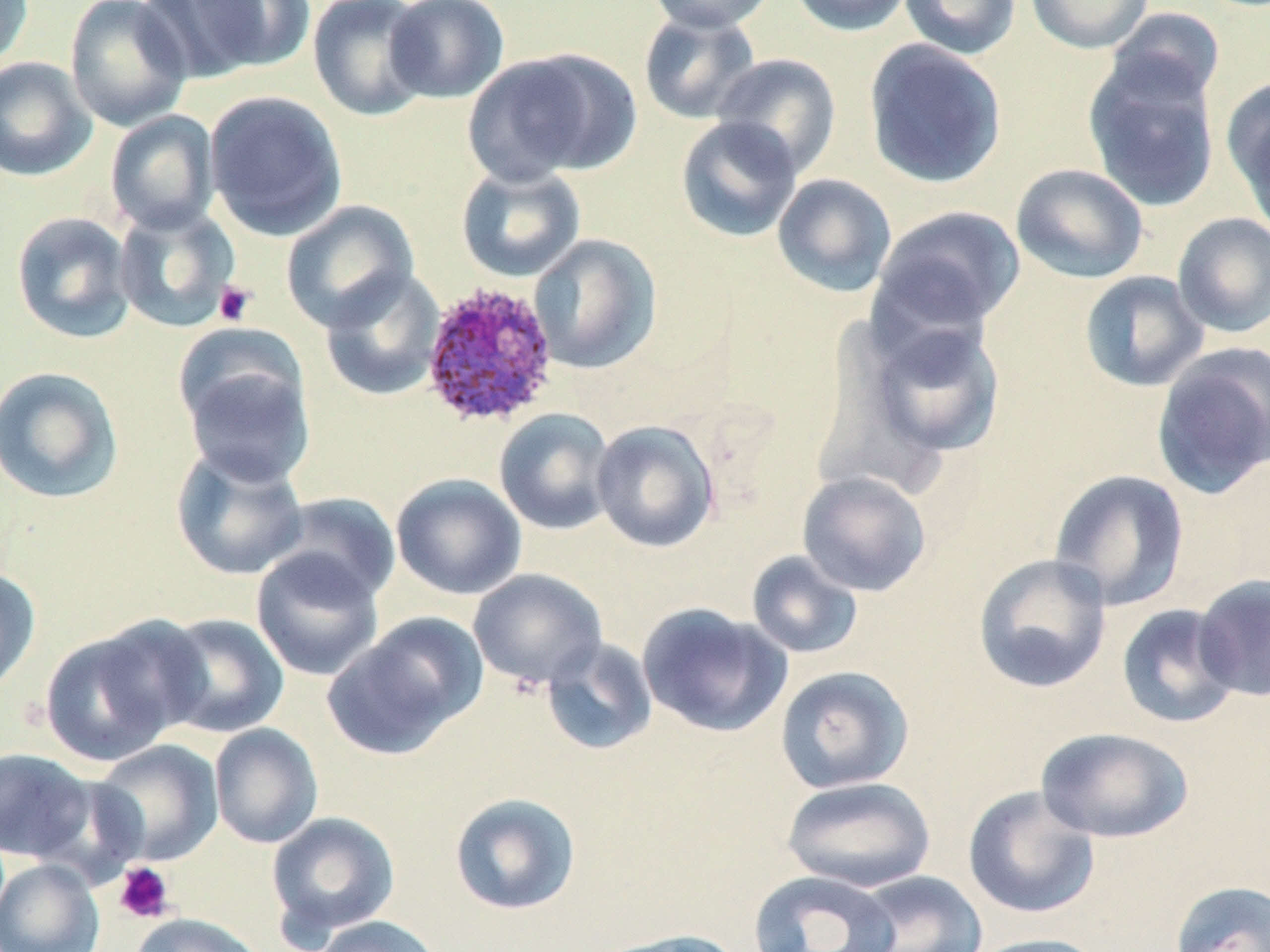
slide-level diagnosis = Plasmodium ovale
modality = optical microscopy
preparation = thin blood smear
field of view = one of a larger specimen
Plasmodium ovale-infected red blood cell locations = approximate bounding boxes as (x1,y1)-(x2,y2) corner pairs in pixels: (420,280)-(560,430)
stain = May-Grünwald-Giemsa
image size = 1270×952 pixels
uninfected red blood cell locations = approximate bounding boxes as (x1,y1)-(x2,y2) corner pairs in pixels: (0,0)-(33,70), (64,0)-(193,131), (152,0)-(314,79), (307,0)-(434,121), (384,0)-(510,104), (645,0)-(777,33), (787,0)-(917,36), (898,0)-(1022,60), (1025,0)-(1153,54), (1107,7)-(1226,107), (638,9)-(761,125), (863,39)-(1007,189), (464,47)-(638,184), (711,52)-(842,176), (0,56)-(97,182), (1083,59)-(1221,213), (1222,77)-(1270,228), (204,90)-(348,240), (104,110)-(220,235), (675,115)-(803,242), (454,162)-(586,282), (1010,163)-(1149,284), (772,173)-(897,297), (280,200)-(419,332), (113,203)-(242,333), (871,205)-(1026,334), (10,210)-(136,344), (1172,212)-(1270,338), (528,233)-(662,373), (319,267)-(446,402), (1079,270)-(1209,392), (854,316)-(1008,462), (1151,342)-(1270,498), (178,343)-(317,488), (0,365)-(125,504), (494,407)-(617,535), (590,420)-(720,553), (170,445)-(309,581), (1048,469)-(1190,611), (797,471)-(932,597), (391,473)-(527,600), (268,491)-(401,606), (250,547)-(385,682), (746,550)-(864,659), (973,553)-(1112,694), (0,566)-(41,695), (468,568)-(608,689), (1193,573)-(1270,702), (637,602)-(790,738), (1116,603)-(1243,729), (155,612)-(289,739), (325,613)-(487,759), (38,619)-(198,768), (540,637)-(659,757), (775,665)-(915,793), (209,724)-(323,849), (1036,726)-(1193,843), (91,739)-(224,867), (0,747)-(96,863), (780,775)-(937,893), (962,785)-(1101,920), (448,791)-(582,916), (266,810)-(401,942), (0,858)-(105,952), (748,869)-(900,952), (846,870)-(989,952), (1169,880)-(1270,952), (128,912)-(264,952), (307,915)-(445,952), (594,927)-(747,952), (966,933)-(1110,952)
platelet locations = approximate bounding boxes as (x1,y1)-(x2,y2) corner pairs in pixels: (213,280)-(256,326), (114,862)-(175,923)
magnification = 1000x